Assess for malaria.
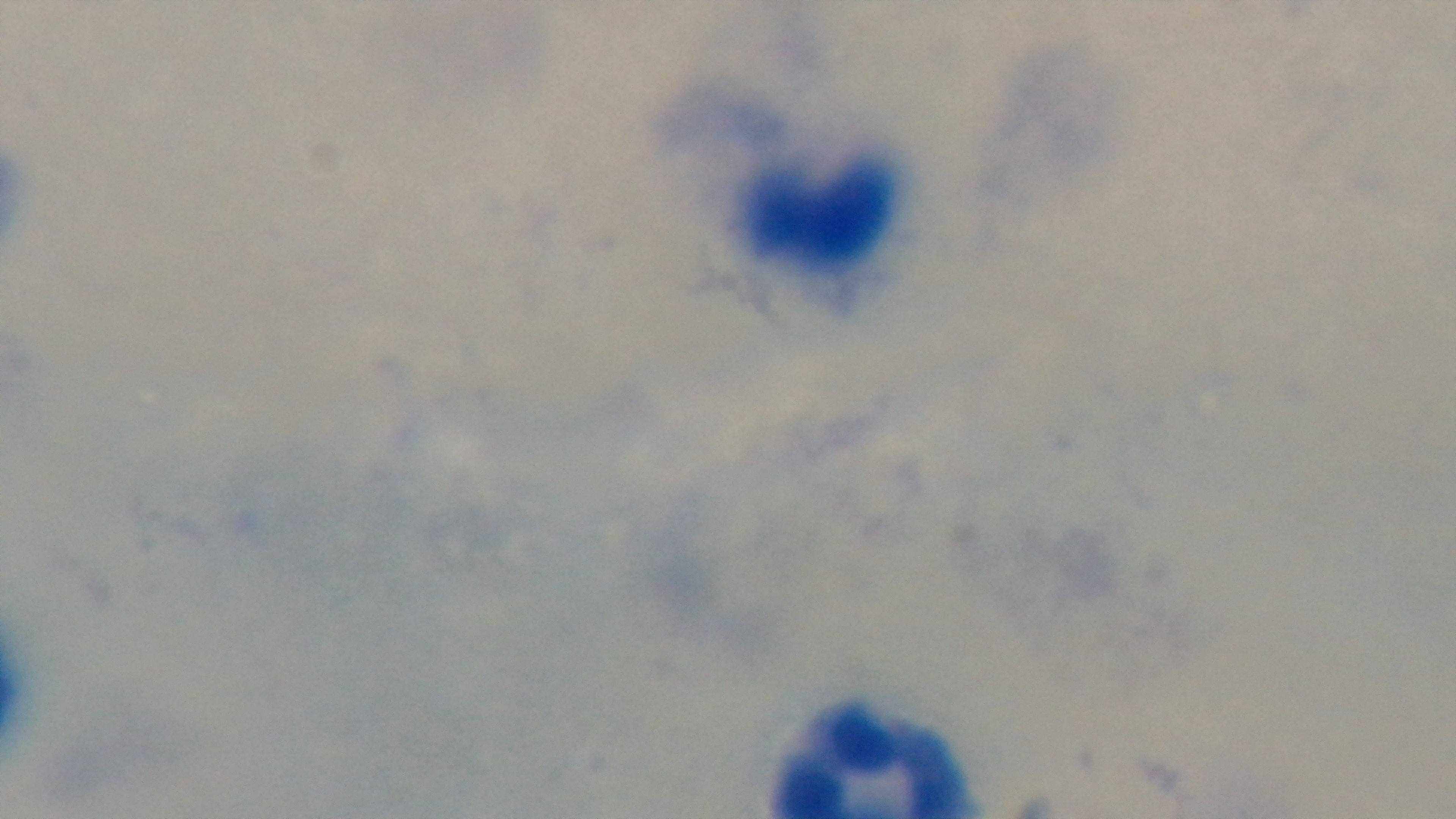

Negative.

Single field of view. Light microscopy. Oil-immersion objective, 100x. Giemsa-stained. Captured with a mounted 4K digital camera. Preparation: thick smear.